Identify the parasite.
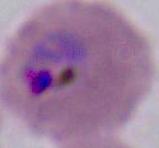

Plasmodium.

400x or 1000x magnification. Photomicrograph.